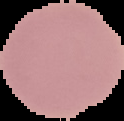
Segmented cell region on a black background. Malaria status: uninfected. Image is 124×121 pixels. From a thin blood smear.